Give the position of every malaria parasite.
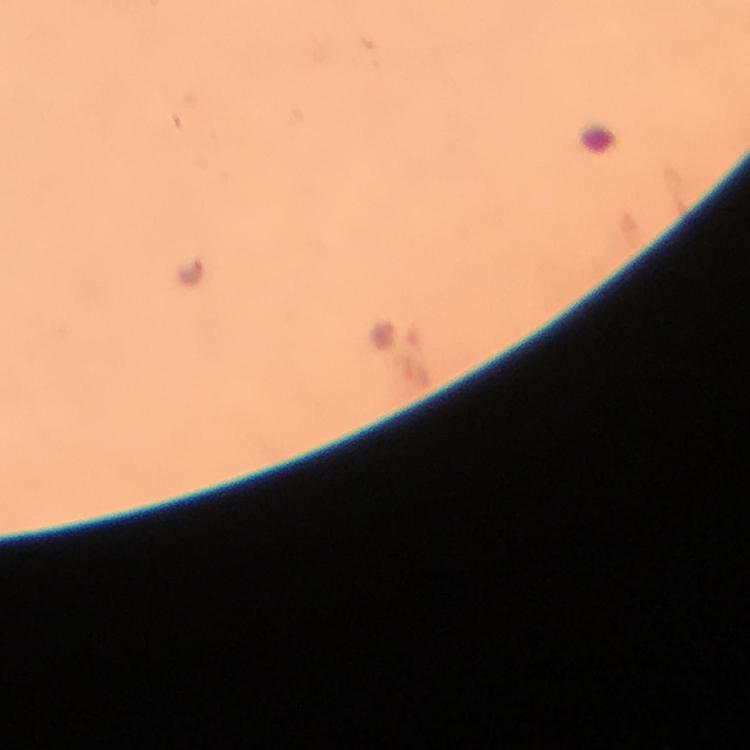

Approximate object centers, in pixels from the top-left corner.
Malaria parasites: (x=191, y=268), (x=380, y=332).

{
  "image_size": "750×750 pixels",
  "stain": "Giemsa",
  "immersion_oil": "used",
  "capture": "smartphone photograph through a microscope",
  "preparation": "thick smear",
  "magnification": "100x",
  "cropped_from": "one field of view",
  "context": "from a diagnostic examination for malaria"
}